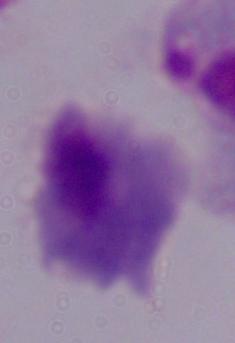

Micrograph. 1000x magnification. A trichomonad is shown.